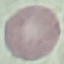
Result: no malaria parasites seen. Giemsa-stained preparation. Photographed with a smartphone camera at the microscope eyepiece. Thin smear of blood. Automatically extracted cell patch, resized to 64 × 64 pixels.